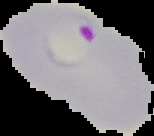

preparation = thin blood smear
image size = 154×136 pixels
malaria status = parasitized
image type = segmented cell region with the area outside set to black